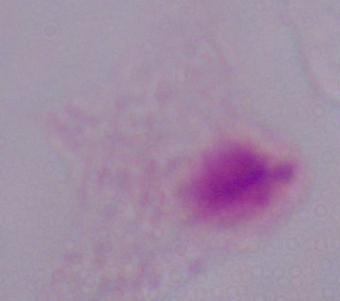
Summary:
  - Identification: trichomonad
  - Modality: micrograph
  - Magnification: 1000x